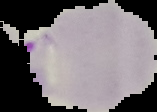 Cell region segmented out of the field of view; the surrounding area is masked to black. Malaria status: parasitized. Image is 157×112 pixels. From a thin blood smear.